Comment on the morphology of the erythrocytes.
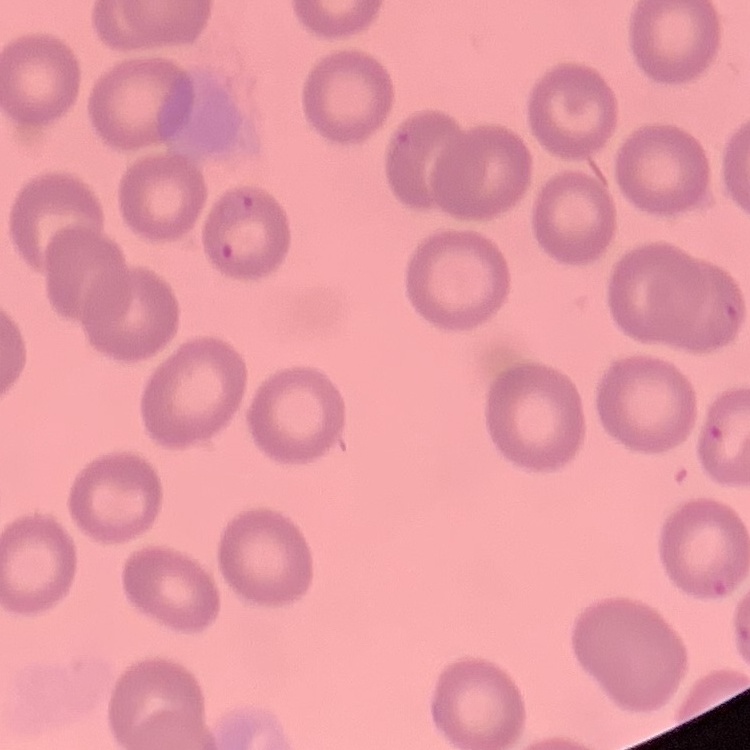
No rouleaux formation.

Summary:
  - Stain: Field's or Giemsa
  - Image type: one tile cut from a larger photomicrograph
  - Preparation: thin blood film